State the blood parasite species.
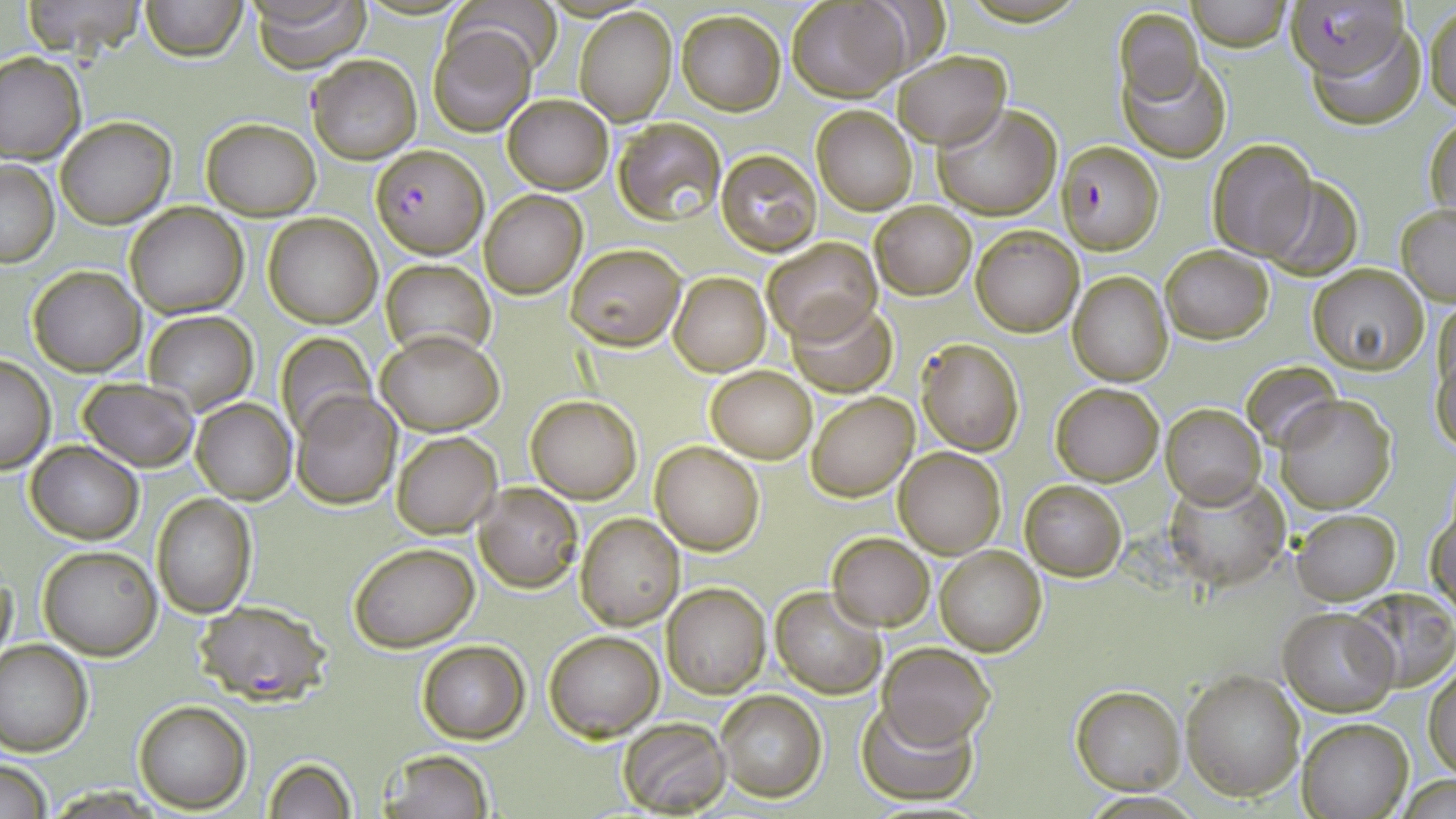

Plasmodium falciparum.

preparation = thin blood smear
Plasmodium falciparum-infected red blood cell locations = approximate bounding boxes as [x1, y1, x2, y2] in pixels: [1292, 0, 1414, 93], [1057, 141, 1163, 254], [373, 145, 486, 257], [193, 601, 330, 704]
modality = optical microscopy
image size = 1456×819 pixels
field of view = one of a larger specimen
magnification = 1000x
uninfected red blood cell locations = approximate bounding boxes as [x1, y1, x2, y2] in pixels: [18, 0, 149, 58], [140, 0, 246, 62], [248, 0, 370, 71], [444, 0, 561, 75], [788, 0, 911, 102], [1189, 0, 1291, 52], [1424, 3, 1456, 114], [574, 7, 676, 125], [1114, 7, 1204, 105], [677, 10, 785, 114], [1308, 23, 1426, 131], [428, 24, 536, 136], [894, 51, 1009, 149], [0, 52, 85, 163], [1118, 53, 1230, 162], [306, 54, 421, 164], [503, 94, 612, 193], [933, 102, 1060, 219], [811, 104, 918, 215], [1425, 111, 1455, 225], [55, 117, 175, 228], [201, 117, 321, 219], [611, 117, 725, 225], [1207, 139, 1316, 259], [715, 148, 822, 257], [1, 159, 59, 267], [1260, 176, 1364, 278], [480, 190, 586, 298], [125, 202, 249, 318], [871, 202, 976, 300], [1396, 205, 1456, 304], [264, 211, 382, 327], [970, 225, 1084, 336], [761, 237, 882, 344], [567, 244, 686, 350], [1160, 245, 1273, 344], [382, 258, 495, 366], [1308, 264, 1429, 373], [28, 265, 146, 375], [668, 272, 770, 375], [1067, 272, 1174, 387], [786, 299, 898, 398], [142, 309, 258, 415], [1432, 321, 1455, 452], [377, 328, 504, 436], [276, 332, 375, 440], [916, 337, 1025, 455], [0, 358, 53, 472], [1244, 359, 1339, 450], [706, 365, 817, 462], [77, 377, 198, 470], [1050, 383, 1163, 485], [291, 390, 401, 509], [807, 392, 919, 501], [526, 394, 642, 504], [1276, 394, 1395, 514], [192, 398, 295, 504], [1159, 402, 1266, 509], [391, 431, 501, 537], [650, 440, 765, 555], [25, 441, 143, 544], [895, 448, 1005, 558], [1165, 473, 1289, 588], [1019, 479, 1128, 581], [474, 483, 582, 592], [152, 494, 256, 619], [1428, 498, 1456, 615], [1291, 509, 1400, 604], [576, 512, 684, 628], [827, 533, 934, 630], [350, 542, 479, 652], [37, 544, 162, 660], [934, 544, 1048, 657], [0, 561, 17, 675], [663, 583, 769, 697], [770, 585, 886, 698], [1347, 587, 1456, 692], [1278, 604, 1399, 715], [544, 630, 663, 740], [0, 639, 93, 755], [416, 641, 529, 743], [878, 642, 996, 748], [1426, 664, 1456, 779], [1181, 669, 1306, 800], [1070, 685, 1186, 795], [714, 688, 827, 803], [855, 699, 978, 802], [132, 700, 250, 812], [616, 716, 732, 815], [1297, 717, 1414, 819], [376, 750, 494, 819], [263, 755, 358, 819], [0, 760, 51, 819], [1400, 775, 1456, 817]
stain = May-Grünwald-Giemsa